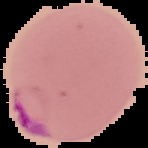
Summary:
  - Preparation: thin blood film
  - Image type: segmented cell region on a black background
  - Malaria status: parasitized
  - Image size: 148×148 pixels